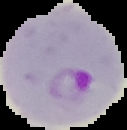
image type = segmented cell region with the area outside set to black
image size = 127×130 pixels
preparation = thin blood film
malaria status = parasitized